Give the extent of all Plasmodium malariae-infected red blood cells.
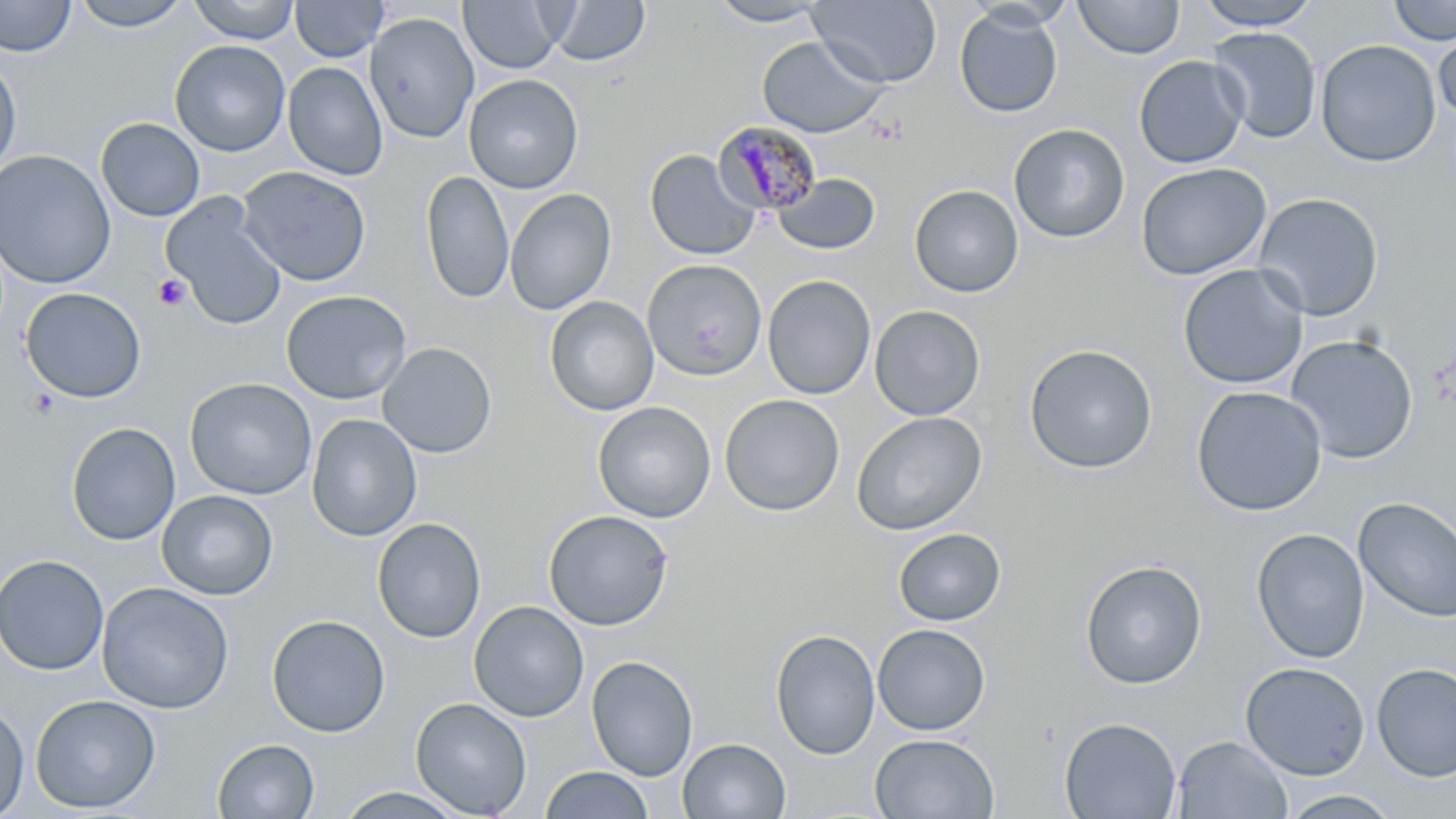
Approximate bounding boxes as (x1, y1, x2, y2) in pixels.
Plasmodium malariae-infected red blood cells: (711, 121, 823, 216).

Summary:
  - Platelet locations: (152, 275, 191, 312), (26, 387, 61, 420)
  - Uninfected red blood cell locations: (0, 0, 76, 58), (69, 0, 193, 32), (187, 0, 300, 44), (290, 0, 389, 62), (458, 0, 567, 74), (551, 0, 652, 67), (704, 0, 833, 27), (808, 0, 942, 87), (1194, 0, 1323, 30), (1388, 0, 1455, 46), (1074, 1, 1185, 59), (954, 8, 1063, 118), (364, 12, 480, 144), (1433, 26, 1456, 122), (1207, 27, 1321, 143), (757, 35, 888, 138), (1315, 39, 1441, 167), (169, 40, 290, 157), (0, 54, 22, 179), (1134, 55, 1249, 169), (282, 62, 388, 180), (463, 74, 584, 194), (96, 118, 205, 222), (1008, 123, 1130, 243), (644, 149, 761, 261), (0, 150, 116, 290), (1135, 162, 1272, 281), (237, 166, 372, 287), (420, 170, 515, 304), (772, 173, 879, 256), (909, 184, 1024, 298), (505, 189, 616, 316), (1252, 192, 1384, 321), (161, 193, 287, 331), (642, 259, 767, 380), (1177, 264, 1310, 390), (763, 275, 875, 399), (20, 287, 147, 404), (281, 290, 411, 405), (545, 297, 659, 415), (869, 305, 985, 420), (1285, 334, 1419, 464), (377, 342, 497, 458), (1024, 344, 1158, 474), (184, 377, 318, 500), (1191, 386, 1327, 516), (719, 394, 845, 517), (593, 401, 716, 523), (851, 411, 987, 536), (307, 414, 422, 542), (65, 422, 181, 546), (156, 489, 278, 600), (1353, 496, 1456, 623), (543, 509, 673, 631), (372, 517, 486, 643), (893, 528, 1006, 626), (1251, 528, 1370, 664), (0, 553, 109, 675), (1079, 559, 1207, 689), (96, 582, 234, 714), (469, 600, 590, 722), (266, 614, 390, 737), (872, 624, 991, 735), (770, 629, 880, 760), (586, 655, 698, 781), (1239, 661, 1370, 780), (1371, 662, 1456, 782), (29, 694, 161, 814), (410, 697, 532, 818), (0, 701, 30, 818), (1059, 716, 1182, 819), (869, 733, 1000, 818), (1172, 735, 1293, 819), (677, 737, 791, 818), (212, 738, 320, 818), (540, 765, 654, 819), (333, 787, 470, 819), (1278, 789, 1404, 818)
  - Slide-level diagnosis: Plasmodium malariae
  - Field of view: single
  - Modality: light microscopy
  - Image size: 1456×819 pixels
  - Stain: May-Grünwald-Giemsa
  - Preparation: thin blood film
  - Magnification: 1000x